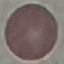
Summary:
  - Malaria status: uninfected
  - Preparation: thin blood smear
  - Stain: Giemsa
  - Image type: cell patch, automatically extracted from a larger field of view and resized to 64 × 64 pixels
  - Capture: smartphone camera at the microscope eyepiece